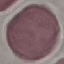
{
  "malaria_status": "uninfected",
  "image_type": "cell patch, automatically extracted from a larger field of view and resized to 64 × 64 pixels",
  "stain": "Giemsa",
  "preparation": "thin smear",
  "capture": "smartphone camera at the microscope eyepiece"
}